State the blood parasite species.
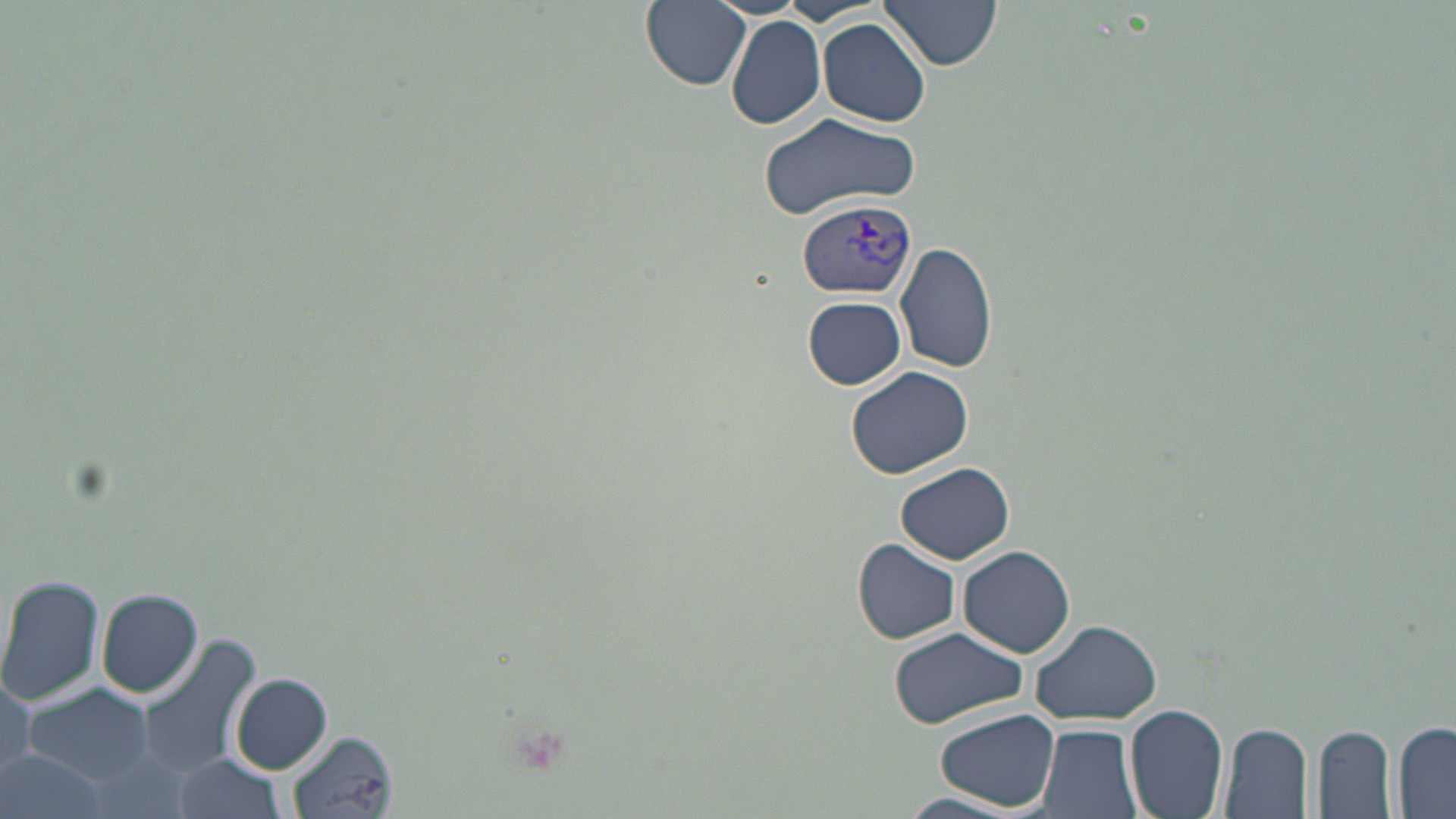

Plasmodium vivax.

Summary:
  - Coordinate format: approximate bounding boxes as (x1, y1, x2, y2) in pixels
  - Uninfected red blood cell locations: (644, 0, 753, 92), (877, 0, 1002, 71), (725, 15, 827, 129), (817, 19, 934, 126), (759, 111, 923, 219), (895, 240, 997, 373), (803, 296, 906, 388), (845, 364, 973, 479), (895, 462, 1015, 564), (853, 539, 959, 645), (958, 545, 1075, 659), (0, 572, 107, 709), (96, 588, 204, 698), (1031, 618, 1163, 727), (887, 626, 1026, 728), (133, 634, 262, 777), (0, 669, 35, 780), (232, 672, 332, 775), (21, 685, 155, 784), (1126, 702, 1229, 819), (936, 707, 1059, 811), (1391, 720, 1456, 817), (1220, 722, 1313, 817), (1035, 723, 1143, 819), (1314, 725, 1397, 818), (288, 731, 397, 817), (1, 749, 110, 819), (173, 756, 284, 818), (891, 794, 1037, 819)
  - Plasmodium vivax-infected red blood cell locations: (797, 199, 916, 299)
  - Stain: May-Grünwald-Giemsa
  - Modality: optical microscopy
  - Image size: 1456×819 pixels
  - Magnification: 1000x
  - Preparation: thin blood film
  - Field of view: one of a larger specimen